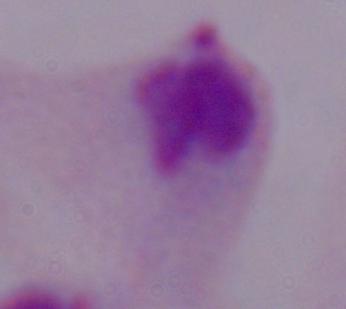
Summary:
  - Modality: photomicrograph
  - Identification: trichomonad
  - Magnification: 1000x